Name the parasite shown.
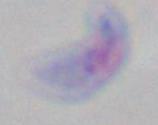
This is Toxoplasma gondii.

modality = photomicrograph
magnification = 1000x